State which parasite is depicted.
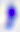
Toxoplasma gondii.

Summary:
  - Modality: photomicrograph
  - Magnification: 400x